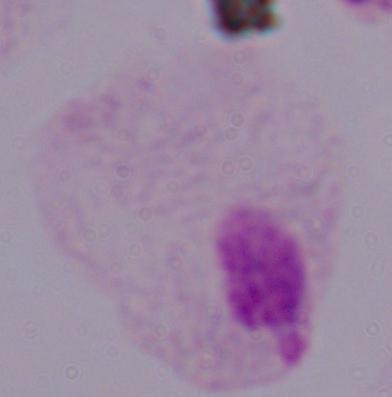

Summary:
  - Identification: trichomonad
  - Modality: micrograph
  - Magnification: 1000x